Assess the morphology of the erythrocytes.
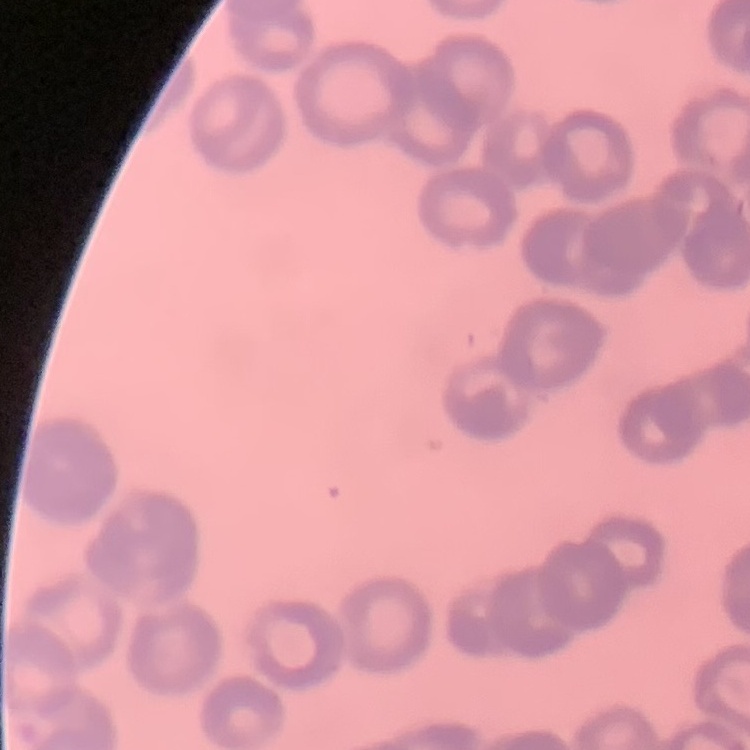

Rouleaux formation.

Thin blood smear. Square crop of a larger photomicrograph. Stained with either Field's or Giemsa.